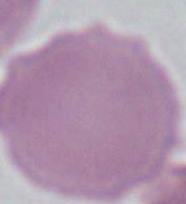

Summary:
  - Modality: micrograph
  - Identification: erythrocyte
  - Magnification: 1000x